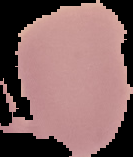

preparation: thin blood smear
image_type: cell region segmented out of the field of view; surrounding area masked to black
result: no malaria parasites detected
image_size: 133×157 pixels